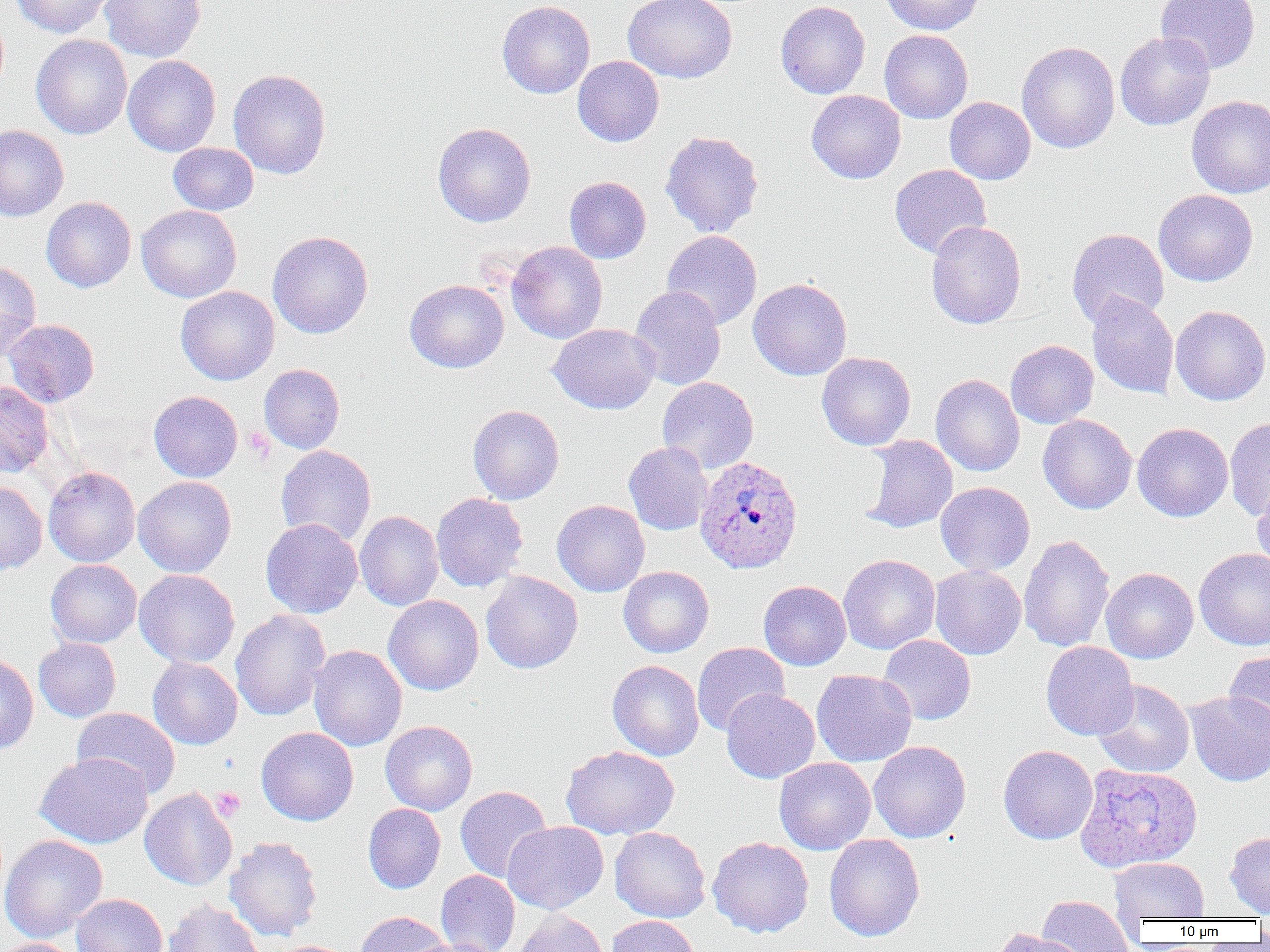
Plasmodium ovale-infected red blood cell locations = approximate bounding boxes as [x1, y1, x2, y2] in pixels: [695, 454, 804, 573], [1075, 763, 1202, 873]
slide-level diagnosis = Plasmodium ovale
platelet locations = approximate bounding boxes as [x1, y1, x2, y2] in pixels: [244, 427, 275, 462], [210, 786, 245, 822]
modality = light microscopy
field of view = single
magnification = 1000x
image size = 1270×952 pixels
uninfected red blood cell locations = approximate bounding boxes as [x1, y1, x2, y2] in pixels: [10, 0, 114, 38], [99, 0, 205, 62], [623, 0, 737, 83], [881, 0, 985, 35], [1156, 0, 1260, 74], [496, 1, 595, 98], [775, 1, 870, 99], [879, 29, 973, 123], [1115, 31, 1215, 131], [31, 34, 132, 139], [1017, 41, 1120, 154], [122, 55, 221, 156], [573, 56, 664, 147], [228, 69, 331, 179], [806, 90, 906, 184], [1186, 95, 1270, 198], [944, 97, 1036, 184], [432, 122, 536, 227], [0, 125, 69, 221], [660, 130, 764, 237], [168, 142, 259, 215], [889, 164, 991, 260], [564, 176, 651, 264], [1153, 189, 1258, 287], [41, 197, 136, 292], [137, 204, 241, 302], [925, 220, 1026, 329], [1066, 228, 1169, 328], [661, 230, 762, 330], [267, 231, 373, 339], [506, 241, 608, 344], [0, 261, 42, 360], [748, 278, 852, 381], [404, 279, 509, 373], [175, 285, 279, 385], [629, 285, 726, 391], [1087, 293, 1179, 399], [1170, 305, 1270, 405], [4, 319, 100, 407], [548, 323, 660, 414], [1005, 340, 1099, 429], [816, 352, 916, 451], [259, 364, 345, 453], [930, 374, 1025, 476], [658, 376, 758, 473], [0, 381, 54, 478], [149, 390, 243, 482], [468, 405, 564, 505], [1037, 414, 1137, 514], [1224, 417, 1270, 521], [1132, 422, 1233, 522], [861, 435, 958, 533], [623, 442, 713, 535], [275, 445, 377, 547], [43, 466, 140, 567], [133, 476, 236, 577], [1252, 479, 1270, 575], [0, 482, 47, 575], [935, 482, 1035, 576], [430, 493, 528, 592], [552, 499, 650, 596], [354, 510, 443, 611], [261, 518, 363, 619], [1019, 534, 1115, 653], [1194, 547, 1270, 650], [838, 553, 940, 654], [45, 559, 142, 648], [929, 564, 1026, 660], [618, 566, 714, 657], [1101, 567, 1198, 664], [134, 569, 239, 668], [1099, 569, 1193, 779], [480, 571, 583, 674], [758, 580, 851, 670], [383, 595, 484, 695], [230, 608, 331, 722], [878, 635, 976, 725], [33, 637, 121, 722], [692, 641, 790, 735], [1041, 641, 1138, 741], [308, 645, 407, 751], [1223, 650, 1270, 740], [0, 652, 39, 755], [147, 657, 242, 750], [607, 660, 704, 760], [811, 669, 917, 766], [1093, 679, 1195, 777], [721, 688, 820, 783], [1184, 691, 1270, 786], [72, 707, 180, 798], [380, 720, 478, 815], [256, 727, 358, 826], [868, 740, 971, 843], [997, 744, 1098, 844], [560, 745, 679, 840], [35, 752, 153, 848], [774, 757, 876, 855], [455, 786, 552, 882], [139, 787, 237, 891], [362, 803, 445, 894], [503, 821, 608, 914], [609, 827, 710, 922], [1225, 831, 1270, 917], [0, 834, 107, 942], [824, 834, 925, 941], [224, 836, 322, 941], [708, 837, 814, 937], [1109, 857, 1209, 922], [435, 870, 521, 952], [71, 894, 168, 952], [1037, 895, 1134, 951], [163, 900, 265, 952], [511, 910, 610, 952], [355, 911, 450, 951], [606, 915, 701, 952], [991, 928, 1092, 952], [406, 937, 501, 952], [0, 938, 81, 952], [267, 940, 358, 952]
preparation = thin blood smear